Locate every malaria parasite.
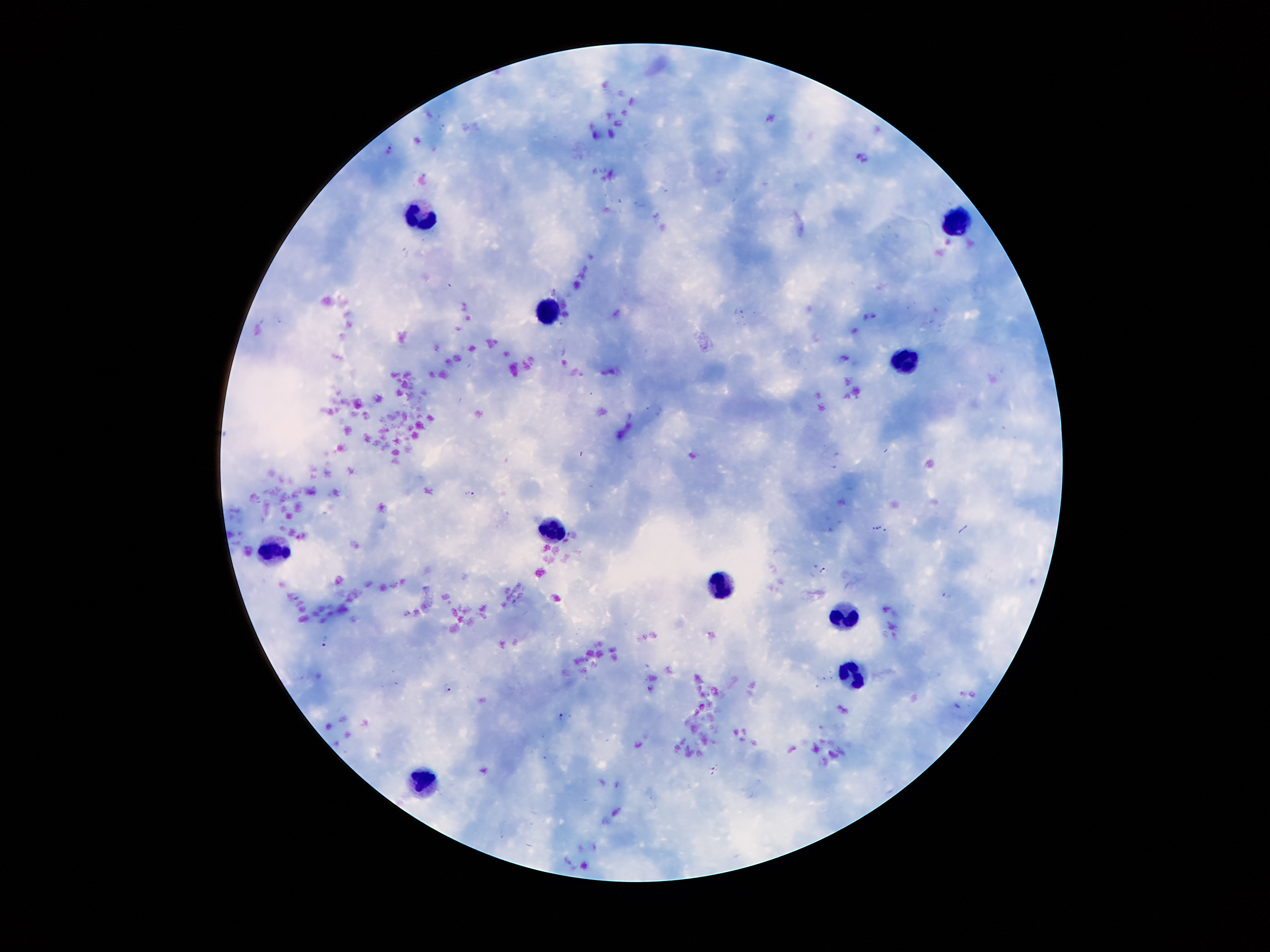
Approximate centers as [x, y] in pixels.
Malaria parasites: [469, 495], [823, 570], [945, 596], [324, 640], [447, 687], [560, 715], [715, 770].

Leukocyte locations: [425, 220], [956, 221], [545, 313], [907, 360], [550, 529], [274, 553], [716, 585], [841, 618], [857, 677], [425, 777]. Thick peripheral-blood smear. One field from this slide. Giemsa stain. Smartphone photograph taken through the microscope eyepiece. Patient malaria status: positive for Plasmodium falciparum. Image is 1270×952 pixels. 100x magnification.